Locate every blood parasite and identify its species.
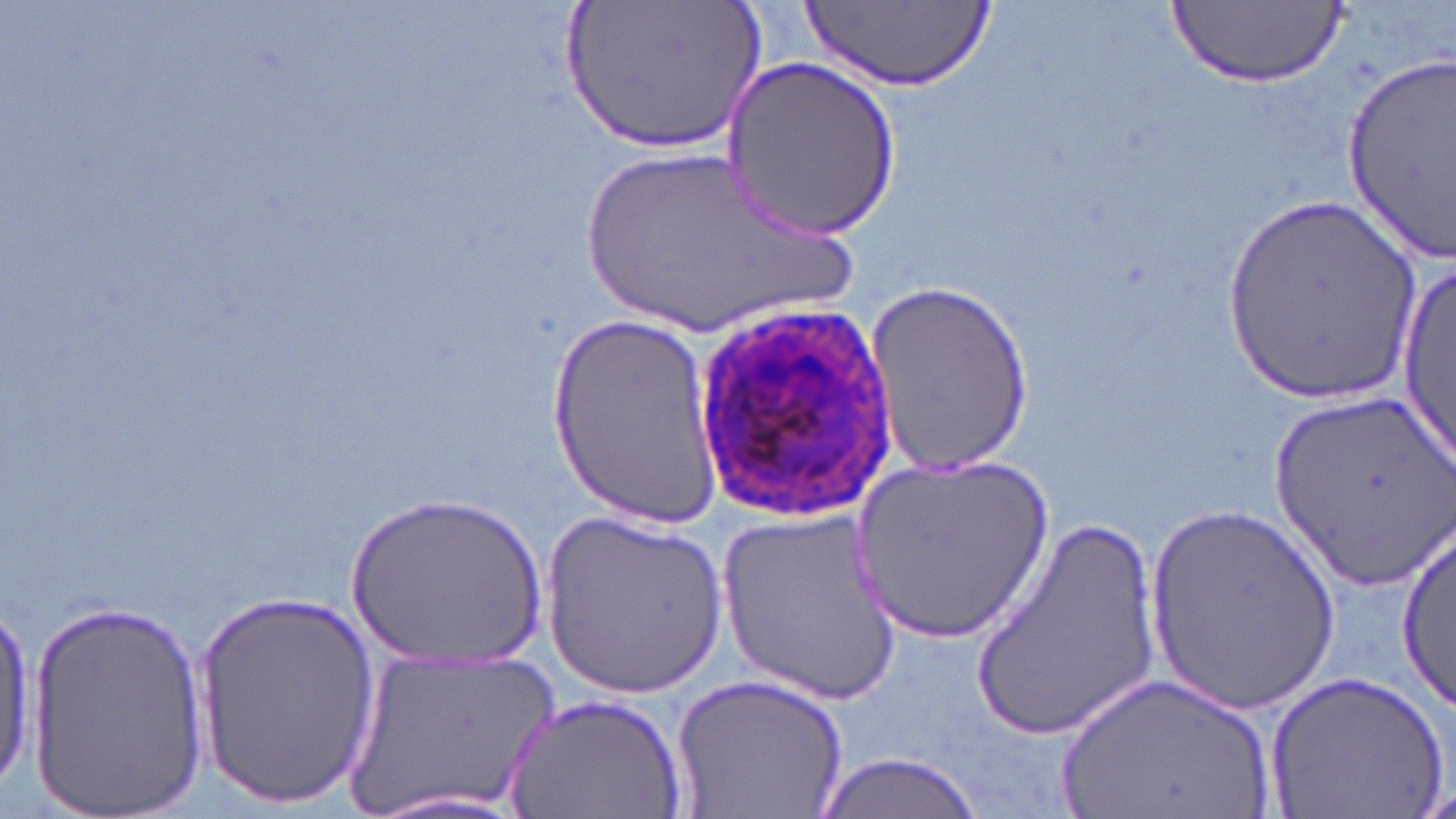

Approximate bounding boxes as (x1, y1, x2, y2) in pixels.
Plasmodium ovale-infected red blood cells: (688, 302, 900, 518).
No Plasmodium falciparum, Plasmodium malariae, Plasmodium vivax, Babesia divergens, or Trypanosoma brucei observed.

Uninfected red blood cell locations: (565, 0, 767, 157), (1168, 0, 1347, 87), (807, 3, 991, 91), (1338, 46, 1455, 266), (722, 57, 906, 239), (565, 144, 867, 340), (1218, 195, 1425, 408), (1395, 248, 1455, 480), (869, 282, 1033, 476), (548, 311, 726, 527), (1270, 393, 1451, 588), (852, 452, 1057, 644), (347, 487, 549, 673), (1146, 499, 1341, 716), (715, 507, 903, 705), (968, 510, 1166, 743), (541, 512, 727, 700), (1397, 532, 1455, 708), (193, 588, 383, 803), (25, 594, 212, 815), (0, 601, 34, 785), (342, 647, 557, 818), (1057, 667, 1280, 819), (673, 672, 848, 819), (1267, 672, 1448, 816), (506, 694, 685, 819), (811, 753, 986, 819), (351, 787, 540, 819). Slide-level diagnosis: Plasmodium ovale. Single field of view. Thin blood film. May-Grünwald-Giemsa-stained preparation. Captured at 1000x magnification. Optical microscopy. Image is 1456×819 pixels.